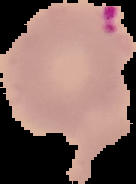

Summary:
  - Preparation: thin blood smear
  - Image size: 136×184 pixels
  - Result: malaria parasites identified
  - Image type: segmented cell region on a black background